Give the extent of all Plasmodium falciparum-infected red blood cells.
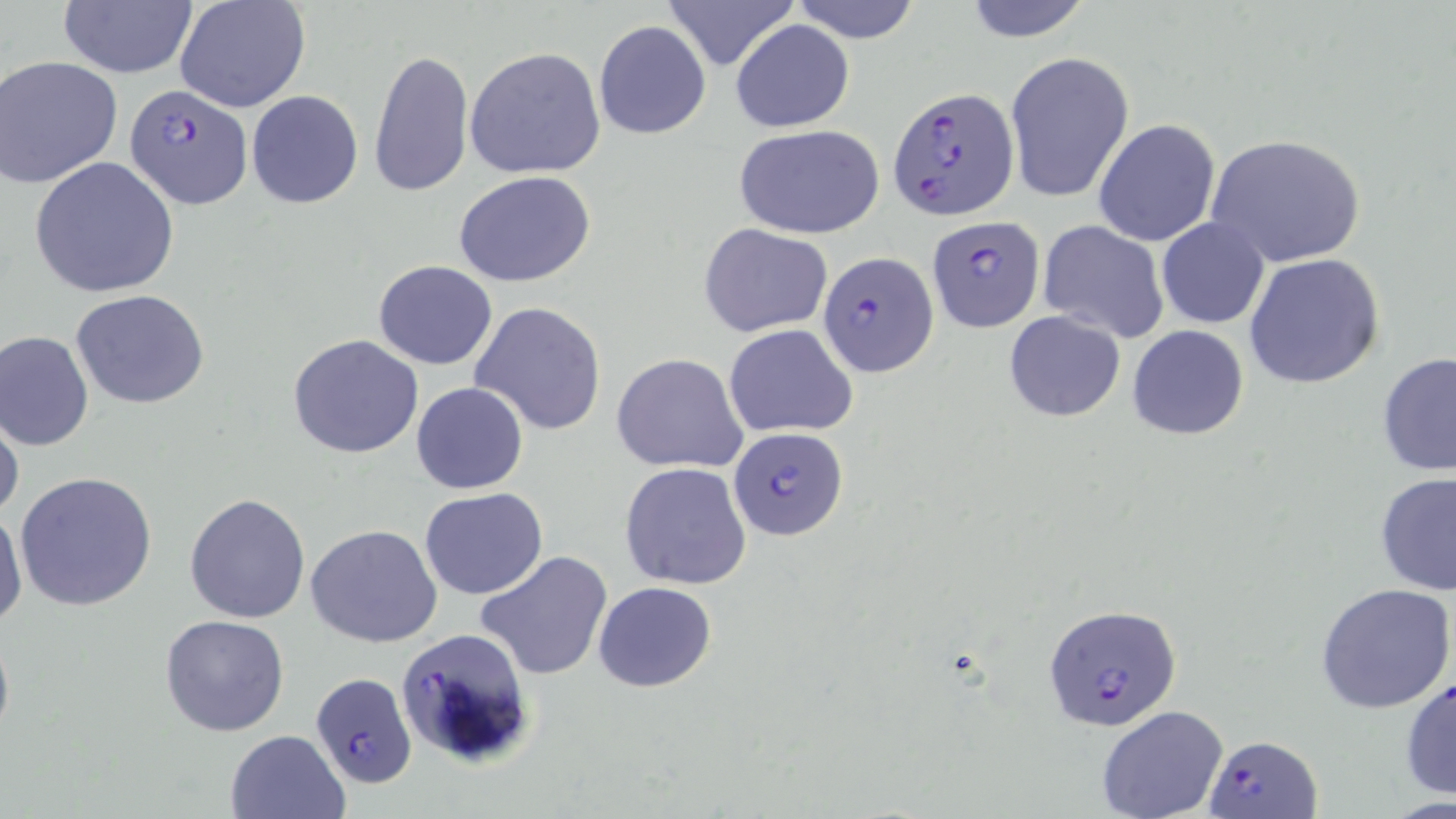
Approximate bounding boxes as [x1, y1, x2, y2] in pixels.
Plasmodium falciparum-infected red blood cells: [123, 81, 254, 211], [888, 89, 1019, 220], [926, 216, 1044, 332], [819, 251, 937, 375], [726, 427, 848, 542], [1044, 604, 1181, 730], [392, 629, 537, 770], [310, 671, 418, 789], [1206, 735, 1321, 817].

{
  "slide_level_diagnosis": "Plasmodium falciparum",
  "preparation": "thin blood film",
  "uninfected_red_blood_cell_locations": "approximate bounding boxes as [x1, y1, x2, y2] in pixels: [174, 0, 311, 114], [661, 0, 800, 71], [790, 0, 923, 44], [959, 0, 1095, 44], [58, 2, 197, 79], [730, 19, 855, 132], [593, 20, 711, 138], [464, 47, 606, 178], [369, 48, 473, 198], [1004, 50, 1134, 203], [1, 55, 124, 187], [246, 90, 363, 208], [1094, 118, 1221, 248], [733, 123, 885, 239], [1206, 132, 1367, 269], [29, 156, 179, 299], [452, 170, 596, 287], [1156, 216, 1269, 329], [1037, 220, 1168, 342], [698, 223, 833, 337], [1244, 252, 1386, 389], [373, 260, 498, 369], [71, 289, 209, 409], [469, 302, 607, 436], [1003, 310, 1126, 423], [725, 323, 858, 438], [1127, 325, 1249, 441], [0, 329, 94, 451], [287, 335, 425, 458], [1377, 351, 1456, 480], [613, 353, 748, 473], [410, 382, 529, 495], [0, 403, 22, 524], [619, 463, 752, 590], [15, 471, 156, 613], [1376, 472, 1456, 595], [419, 488, 547, 600], [185, 493, 311, 623], [1, 503, 27, 636], [306, 524, 442, 648], [475, 551, 614, 682], [594, 581, 717, 693], [1315, 583, 1454, 714], [159, 614, 291, 737], [0, 617, 14, 753], [1400, 674, 1456, 801], [1096, 706, 1229, 819], [225, 730, 349, 819]",
  "image_size": "1456×819 pixels",
  "stain": "May-Grünwald-Giemsa",
  "modality": "optical microscopy",
  "magnification": "1000x",
  "field_of_view": "single"
}